Assess the morphology of the erythrocytes.
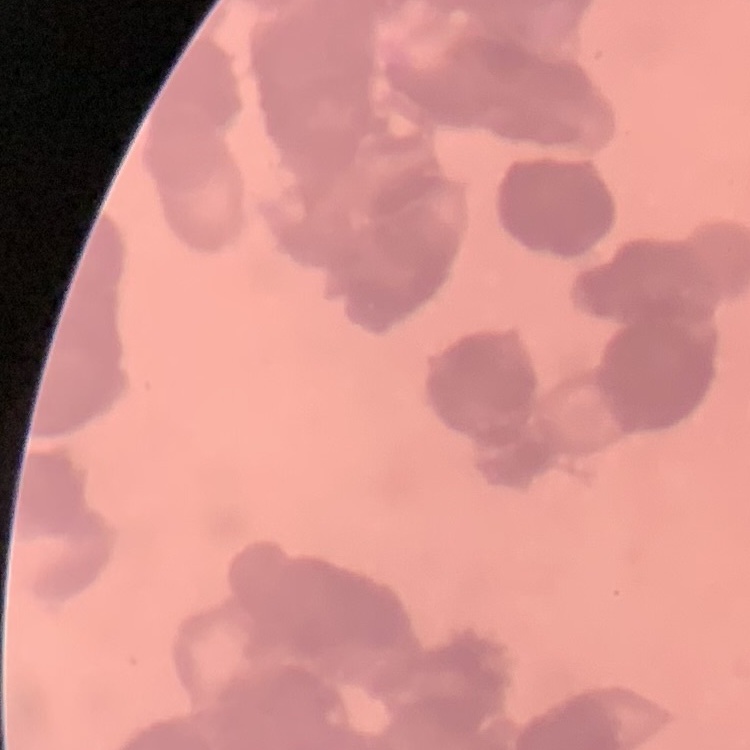

Rouleaux formation.

image type = square crop of a larger photomicrograph
preparation = thin blood film
stain = Field's or Giemsa